Name the parasite shown.
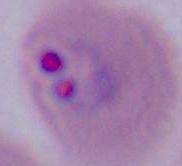

This is Plasmodium.

Summary:
  - Magnification: 400x or 1000x
  - Modality: photomicrograph